Report the malaria status of this cell.
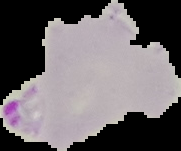
Parasitized.

Summary:
  - Image type: segmented cell region with the area outside set to black
  - Preparation: thin blood smear
  - Image size: 181×151 pixels